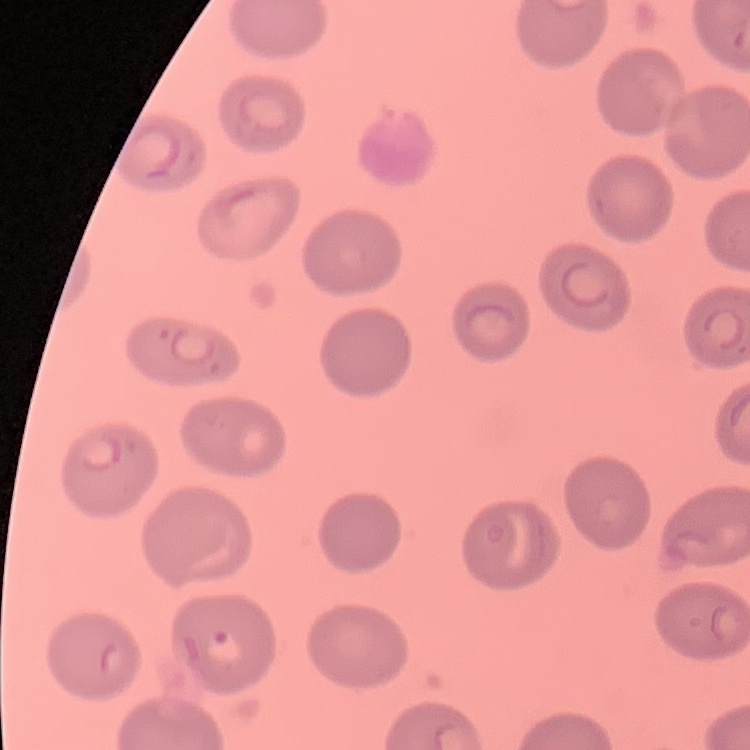
red_blood_cell_morphology: no rouleaux formation
preparation: thin blood smear
stain: Field's or Giemsa
image_type: one tile cut from a larger photomicrograph